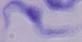
identification = trypanosome
modality = photomicrograph
magnification = 1000x